State which parasite is depicted.
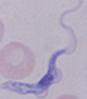

A trypanosome.

Photomicrograph. 1000x magnification.